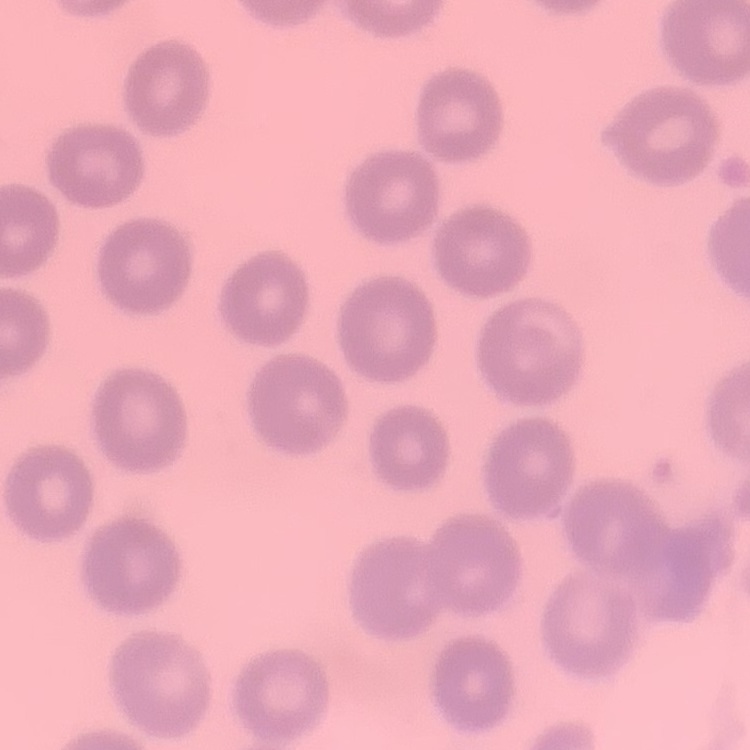

red_blood_cell_morphology: no rouleaux formation
image_type: one tile cut from a larger photomicrograph
stain: Field's or Giemsa
preparation: thin blood smear